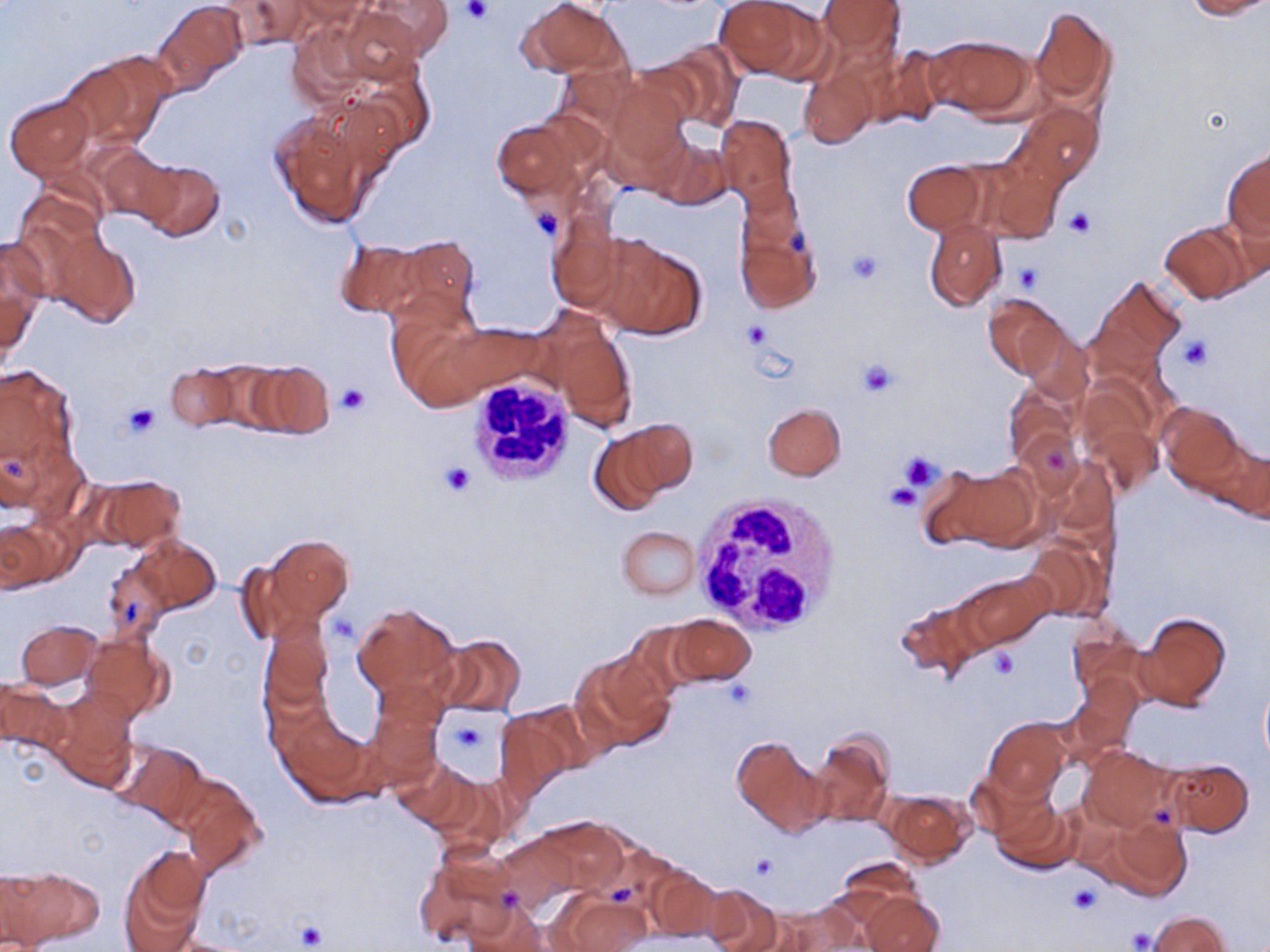 Approximate bounding boxes as [x1, y1, x2, y2] in pixels. Uninfected red blood cell locations: [357, 0, 454, 64], [522, 0, 625, 76], [716, 0, 817, 80], [816, 0, 906, 63], [1183, 0, 1270, 19], [219, 1, 312, 50], [156, 3, 247, 85], [1028, 5, 1117, 107], [330, 8, 425, 85], [927, 34, 1034, 120], [654, 39, 746, 130], [870, 42, 947, 130], [63, 54, 169, 149], [798, 68, 877, 148], [602, 74, 693, 171], [4, 95, 96, 182], [1012, 102, 1101, 186], [266, 110, 379, 230], [716, 113, 797, 208], [492, 118, 586, 204], [647, 129, 733, 206], [94, 146, 181, 229], [1223, 149, 1270, 246], [132, 158, 224, 242], [978, 158, 1066, 242], [903, 161, 986, 235], [731, 196, 821, 315], [547, 217, 644, 317], [923, 218, 1006, 311], [1159, 222, 1253, 304], [47, 230, 141, 329], [388, 233, 481, 327], [592, 233, 708, 340], [0, 238, 46, 358], [334, 238, 419, 320], [1088, 276, 1187, 376], [983, 293, 1066, 378], [386, 307, 502, 409], [543, 318, 638, 429], [437, 323, 547, 400], [1016, 325, 1096, 405], [192, 360, 284, 432], [245, 360, 335, 441], [166, 364, 240, 432], [0, 365, 80, 484], [1004, 384, 1080, 468], [1158, 401, 1246, 491], [763, 402, 845, 480], [1080, 416, 1163, 500], [613, 419, 698, 501], [587, 429, 672, 515], [1193, 432, 1269, 519], [925, 463, 1036, 552], [85, 473, 186, 555], [0, 514, 71, 595], [618, 525, 700, 599], [255, 535, 352, 628], [134, 536, 220, 614], [1019, 539, 1109, 623], [234, 555, 321, 643], [102, 560, 174, 642], [957, 572, 1053, 650], [894, 597, 987, 683], [353, 603, 459, 702], [1134, 612, 1232, 712], [666, 614, 757, 686], [260, 619, 335, 710], [17, 620, 101, 688], [1066, 620, 1148, 701], [82, 634, 171, 723], [433, 634, 526, 718], [573, 651, 677, 752], [1066, 672, 1141, 758], [1259, 675, 1270, 772], [0, 677, 69, 758], [44, 687, 137, 791], [364, 691, 445, 787], [495, 705, 586, 794], [274, 711, 374, 805], [984, 718, 1070, 802], [808, 731, 894, 830], [729, 738, 828, 837], [112, 741, 208, 829], [1078, 746, 1176, 832], [391, 757, 475, 830], [1164, 758, 1255, 837], [428, 772, 510, 855], [180, 780, 267, 878], [885, 791, 973, 866], [989, 792, 1078, 876], [1091, 813, 1194, 901], [531, 818, 631, 900], [119, 852, 207, 951], [417, 854, 517, 946], [641, 859, 726, 945], [2, 866, 99, 948], [699, 883, 785, 952], [863, 892, 943, 952], [559, 896, 650, 951], [766, 903, 859, 952], [458, 906, 560, 951], [1146, 911, 1230, 952]. White blood cell locations: [465, 374, 579, 487], [692, 494, 843, 636]. Platelet locations: [460, 0, 490, 25], [528, 202, 563, 241], [1063, 208, 1097, 238], [843, 247, 884, 286], [1015, 263, 1043, 291], [741, 321, 772, 351], [1175, 333, 1213, 372], [856, 357, 900, 398], [337, 384, 369, 415], [121, 403, 161, 438], [899, 452, 941, 491], [438, 462, 477, 496], [885, 482, 922, 511], [989, 647, 1018, 678], [446, 715, 492, 763], [751, 855, 780, 882], [1068, 884, 1100, 915], [296, 921, 327, 950], [1126, 927, 1155, 950]. Slide-level diagnosis: negative for blood parasites. One field of a larger specimen. Captured at 1000x magnification. May-Grünwald-Giemsa stain. Optical microscopy. Image is 1270×952 pixels. Thin blood film.